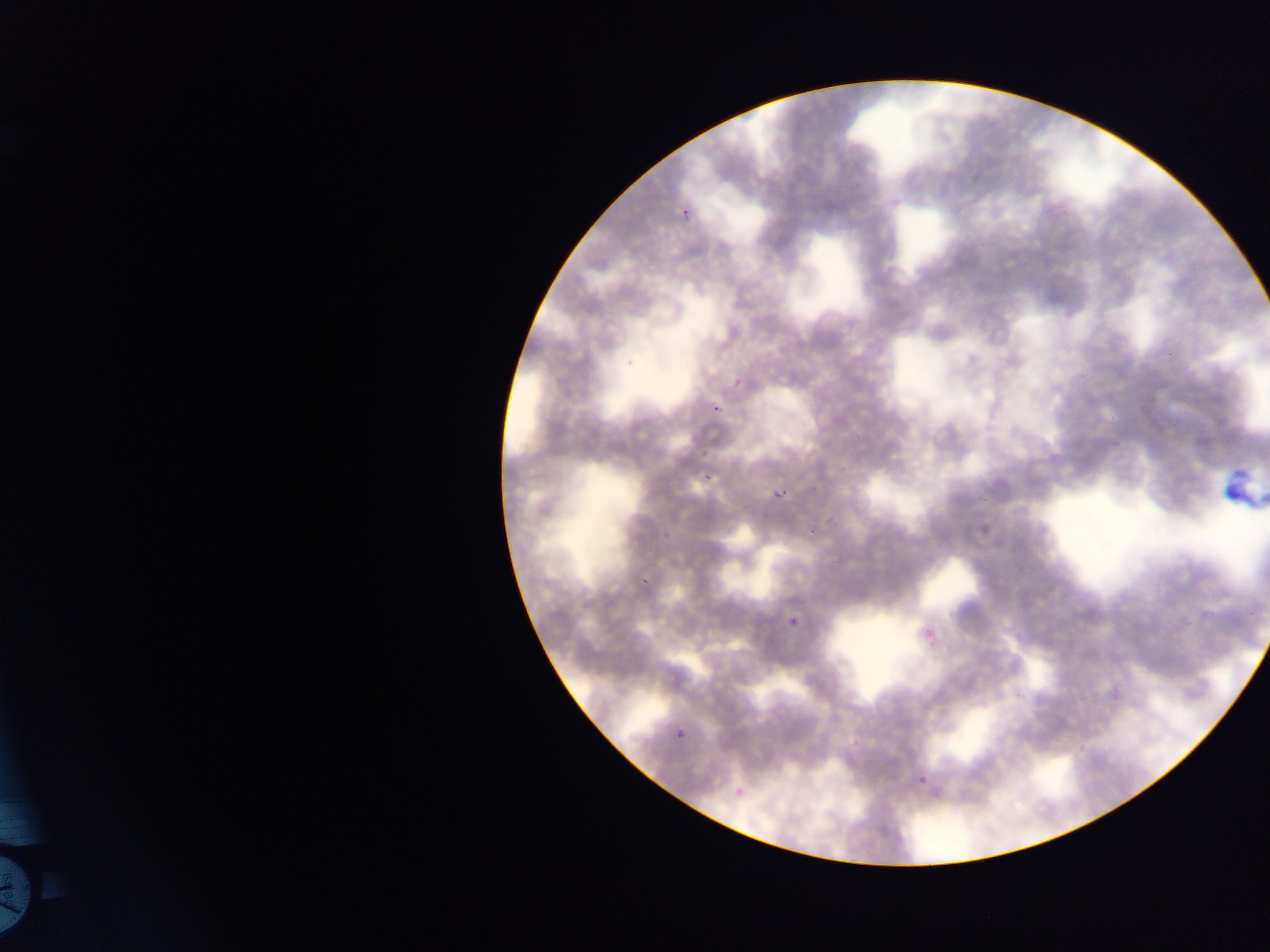

Approximate bounding boxes as [left, top, right, bottom] in pixels. Artifact (stain precipitate or debris) locations: [1217, 465, 1270, 512]. Plasmodium parasite locations: [677, 203, 700, 229], [709, 401, 726, 421], [703, 465, 715, 482], [772, 485, 790, 506], [807, 517, 823, 536], [830, 552, 839, 573], [635, 575, 651, 591], [786, 602, 812, 626], [674, 725, 688, 741], [915, 770, 935, 794]. One field of view. Mobile-phone photograph taken through the microscope. Thin blood film. Sample from Ghana. Image is 1270×952 pixels.